Report the malaria status of this cell.
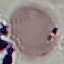

Uninfected.

preparation = thin blood film
capture = smartphone camera at the microscope eyepiece
stain = Giemsa
image type = cell patch, automatically extracted from a larger field of view and resized to 64 × 64 pixels